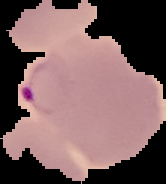 Image is 166×184 pixels. From a thin blood film. The area outside the segmented cell region is set to black. Malaria status: parasitized.